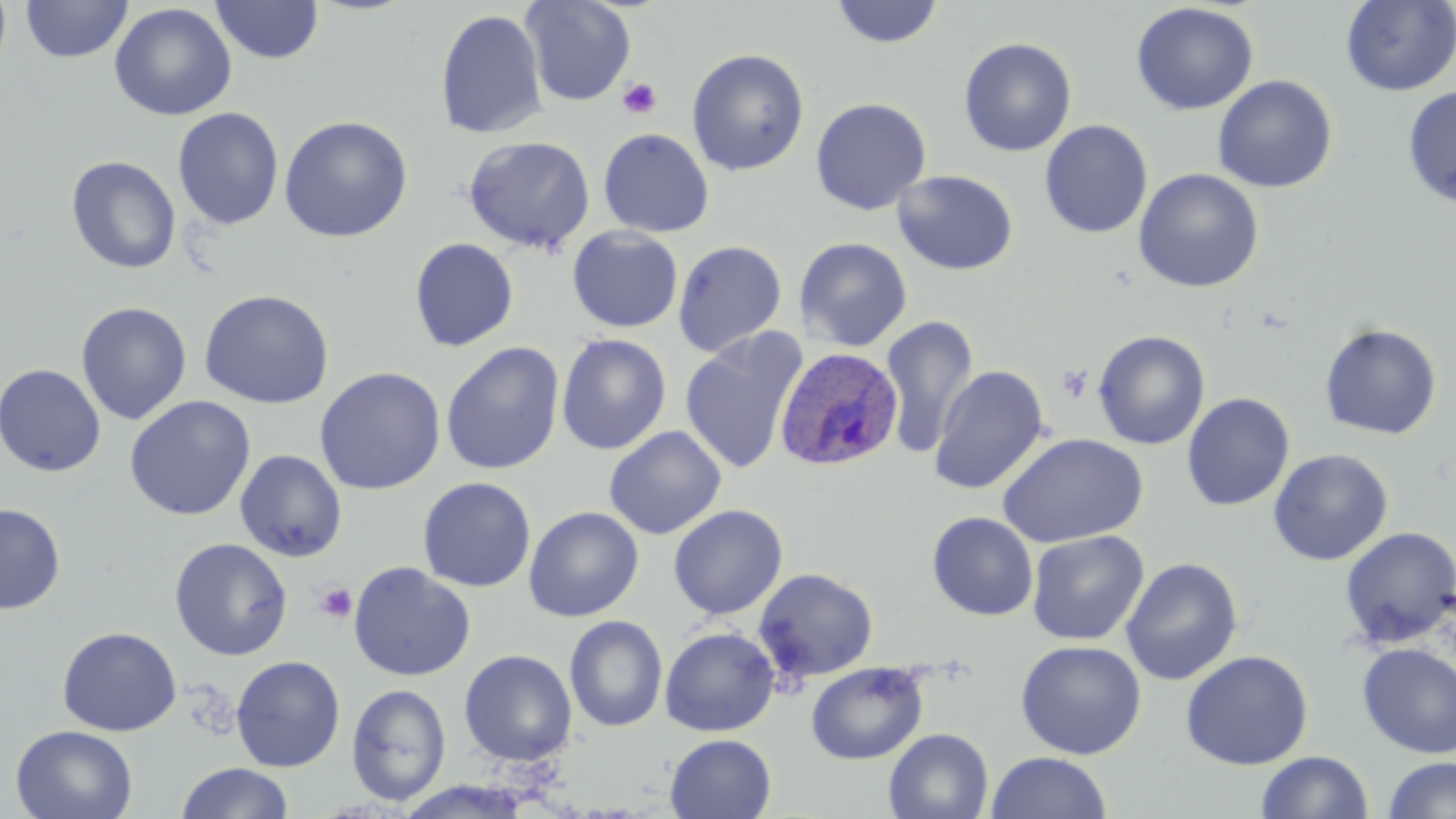
Approximate bounding boxes as [x1, y1, x2, y2] in pixels. Plasmodium ovale-infected red blood cell locations: [775, 347, 904, 472]. Platelet locations: [617, 77, 662, 120], [315, 582, 358, 624]. Uninfected red blood cell locations: [21, 0, 132, 62], [211, 0, 324, 64], [521, 0, 636, 106], [830, 1, 945, 49], [1341, 1, 1456, 96], [1130, 2, 1259, 115], [109, 3, 236, 121], [435, 8, 548, 139], [958, 37, 1077, 157], [686, 48, 810, 176], [1212, 74, 1337, 193], [1402, 85, 1456, 208], [810, 97, 932, 215], [172, 107, 284, 231], [278, 115, 413, 242], [1040, 119, 1154, 239], [598, 128, 714, 238], [463, 135, 595, 255], [66, 155, 181, 274], [1133, 168, 1264, 293], [892, 169, 1019, 275], [567, 226, 682, 332], [795, 236, 913, 351], [409, 237, 519, 352], [673, 239, 787, 357], [199, 289, 335, 409], [75, 301, 192, 424], [879, 315, 979, 458], [1319, 322, 1442, 439], [679, 328, 808, 477], [1093, 330, 1210, 450], [556, 333, 671, 454], [440, 341, 564, 475], [0, 363, 106, 477], [930, 364, 1049, 495], [314, 366, 446, 495], [1182, 392, 1295, 511], [124, 395, 256, 521], [604, 426, 727, 540], [996, 432, 1149, 548], [1268, 448, 1393, 566], [234, 449, 348, 562], [417, 477, 536, 592], [0, 502, 66, 614], [668, 504, 788, 619], [524, 506, 644, 622], [927, 512, 1038, 621], [1339, 525, 1455, 649], [1027, 530, 1149, 645], [169, 537, 293, 661], [1120, 557, 1243, 686], [348, 562, 476, 681], [755, 567, 879, 682], [564, 615, 668, 733], [57, 626, 182, 736], [660, 627, 780, 736], [1015, 640, 1146, 759], [1356, 643, 1456, 759], [459, 649, 578, 767], [1180, 650, 1313, 770], [231, 655, 345, 772], [806, 661, 929, 764], [346, 683, 451, 807], [10, 725, 138, 818], [884, 728, 994, 819], [665, 734, 777, 818], [986, 751, 1112, 819], [1256, 751, 1374, 819], [1384, 757, 1456, 818], [175, 762, 294, 819], [396, 779, 534, 819]. Slide-level diagnosis: Plasmodium ovale. Optical microscopy. Thin blood smear. May-Grünwald-Giemsa stain. 1000x magnification. One field of a larger specimen. Image is 1456×819 pixels.